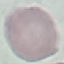
Summary:
  - Result: no malaria parasites detected
  - Stain: Giemsa
  - Capture: smartphone camera at the microscope eyepiece
  - Image type: cell patch, automatically extracted from a larger field of view and resized to 64 × 64 pixels
  - Preparation: thin blood smear